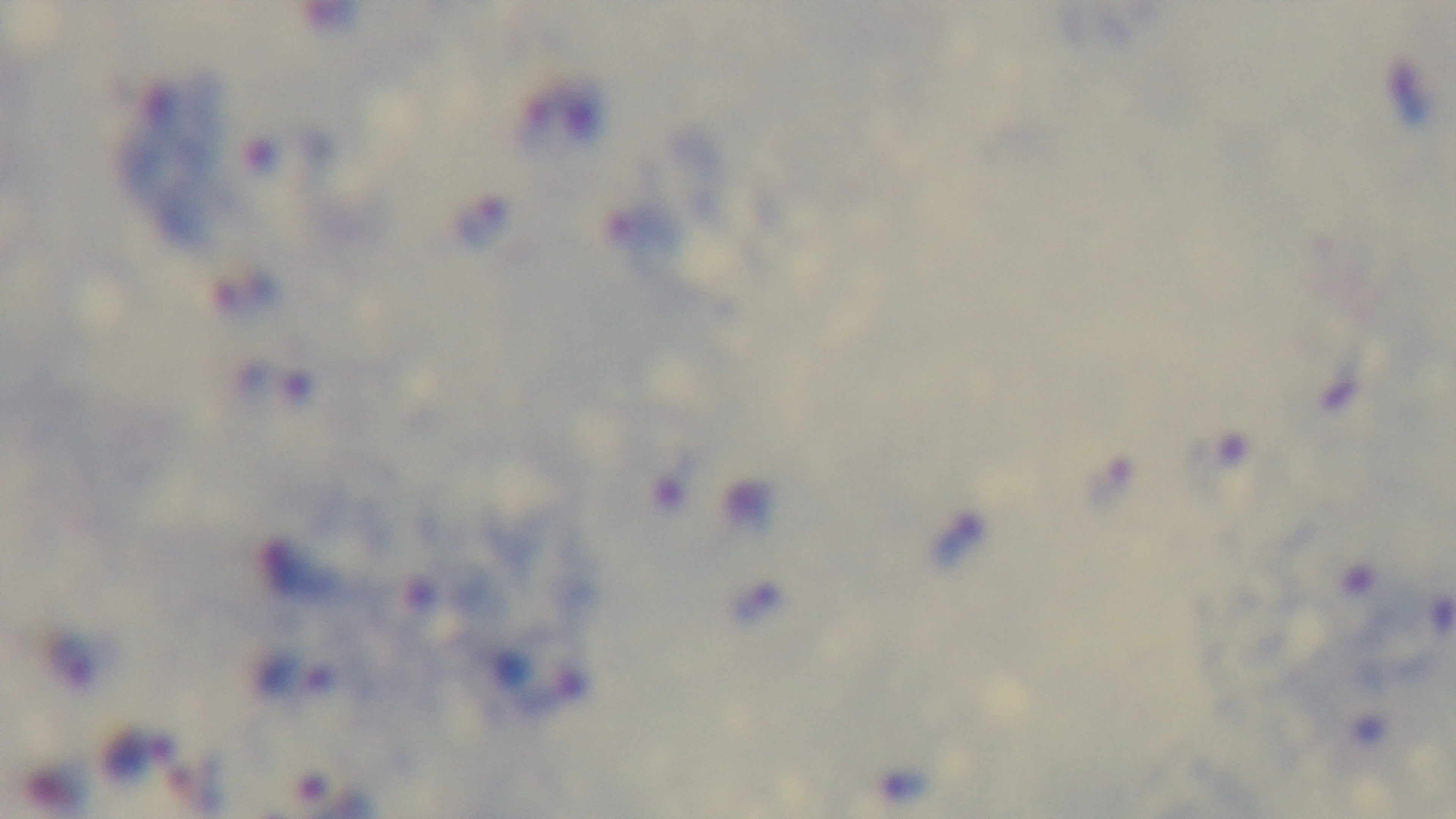
stain = Giemsa
objective = 100x oil immersion
field of view = one from the slide
modality = light microscopy
preparation = thick blood film
capture = mounted 4K digital camera
malaria status = positive